Classify this cell by malaria status.
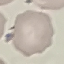
Uninfected.

Cell patch, automatically extracted from a larger field of view and resized to 64 × 64 pixels. Thin smear of blood. Photographed with a smartphone camera at the microscope eyepiece. Giemsa-stained preparation.